State the blood parasite species.
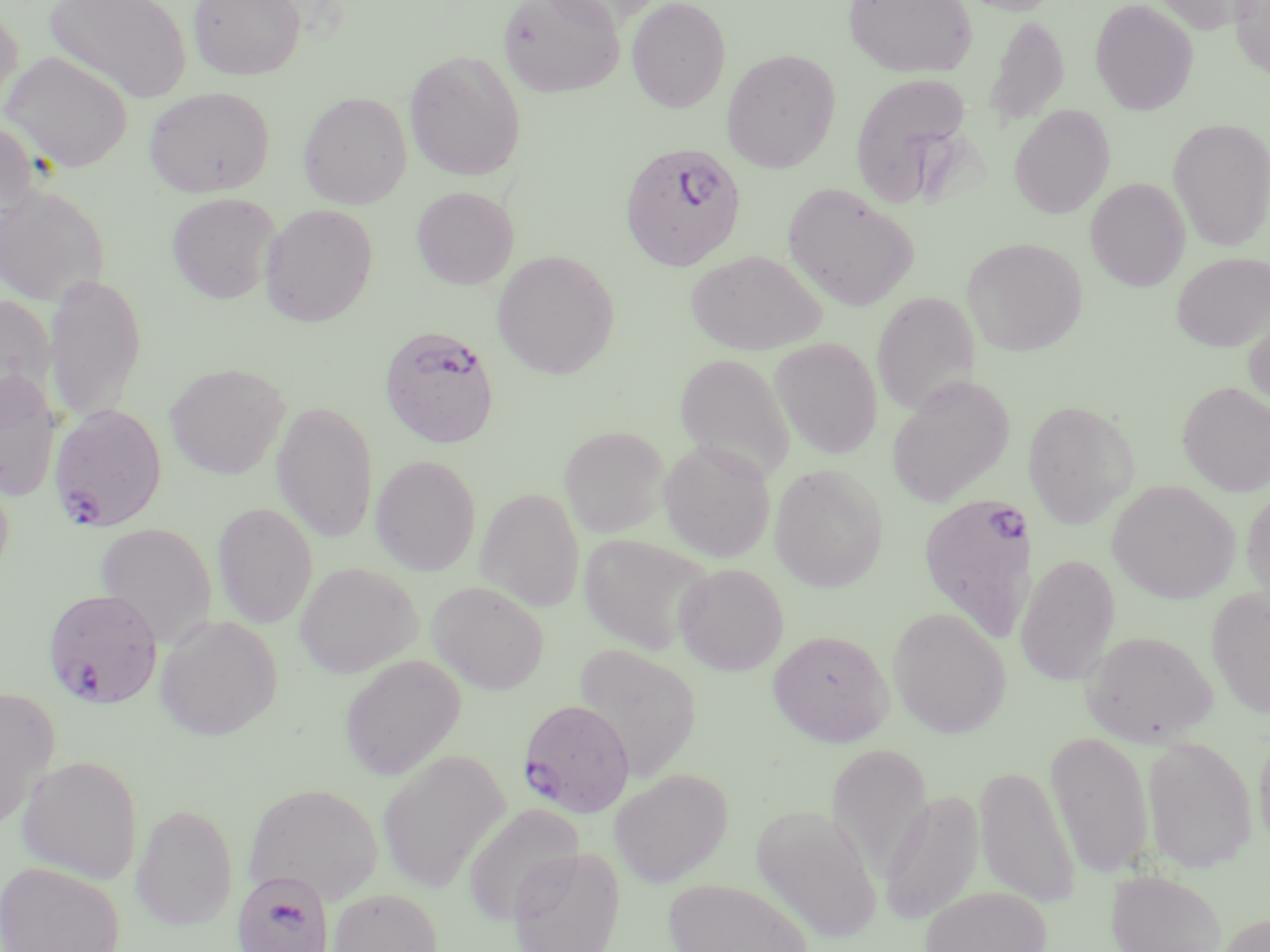
Plasmodium falciparum.

preparation = thin blood film
field of view = single
Plasmodium falciparum-infected red blood cell locations = approximate bounding boxes as [x1, y1, x2, y2] in pixels: [619, 142, 746, 270], [379, 325, 500, 448], [49, 403, 167, 530], [916, 491, 1036, 640], [42, 587, 164, 710], [517, 698, 635, 817], [233, 870, 334, 952]
magnification = 1000x
stain = May-Grünwald-Giemsa
uninfected red blood cell locations = approximate bounding boxes as [x1, y1, x2, y2] in pixels: [44, 0, 191, 105], [188, 0, 305, 80], [497, 0, 624, 98], [626, 0, 731, 113], [843, 0, 977, 79], [953, 0, 1064, 16], [1090, 0, 1199, 116], [1153, 0, 1263, 34], [1230, 0, 1270, 81], [0, 4, 24, 115], [983, 13, 1070, 132], [721, 49, 840, 173], [404, 50, 526, 182], [1, 51, 133, 173], [849, 71, 975, 207], [144, 86, 275, 198], [298, 92, 412, 209], [1008, 104, 1115, 219], [1167, 118, 1270, 251], [0, 120, 40, 230], [1085, 178, 1190, 291], [782, 183, 920, 311], [0, 186, 109, 306], [411, 186, 519, 290], [167, 192, 281, 304], [259, 204, 378, 327], [962, 237, 1087, 356], [686, 249, 827, 355], [492, 250, 619, 379], [1171, 252, 1270, 352], [45, 273, 146, 427], [871, 292, 980, 417], [0, 295, 57, 417], [1244, 311, 1270, 415], [770, 338, 883, 459], [674, 352, 796, 484], [165, 362, 290, 479], [0, 369, 61, 502], [885, 375, 1016, 507], [1178, 381, 1270, 496], [1022, 400, 1139, 528], [271, 401, 379, 544], [559, 425, 669, 537], [659, 440, 776, 562], [371, 455, 482, 575], [0, 461, 15, 584], [769, 463, 888, 591], [1107, 480, 1239, 604], [1241, 485, 1270, 612], [476, 487, 585, 612], [212, 501, 319, 629], [96, 523, 217, 647], [578, 533, 712, 655], [1015, 554, 1121, 686], [294, 562, 422, 678], [673, 563, 788, 675], [427, 581, 550, 695], [1206, 587, 1270, 721], [888, 606, 1011, 739], [154, 615, 283, 741], [768, 629, 893, 746], [1081, 629, 1218, 746], [573, 643, 701, 782], [339, 654, 466, 781], [0, 686, 60, 831], [1253, 721, 1270, 857], [1045, 731, 1154, 879], [1142, 735, 1257, 873], [827, 743, 932, 883], [377, 749, 509, 893], [17, 754, 143, 884], [975, 764, 1079, 908], [609, 768, 733, 887], [244, 783, 383, 905], [879, 789, 984, 925], [131, 802, 239, 931], [463, 803, 584, 925], [750, 804, 882, 944], [507, 846, 626, 952], [0, 860, 124, 952], [1106, 869, 1227, 952], [663, 879, 813, 952], [920, 885, 1051, 952], [329, 887, 443, 952], [1212, 913, 1270, 952]
modality = light microscopy
image size = 1270×952 pixels